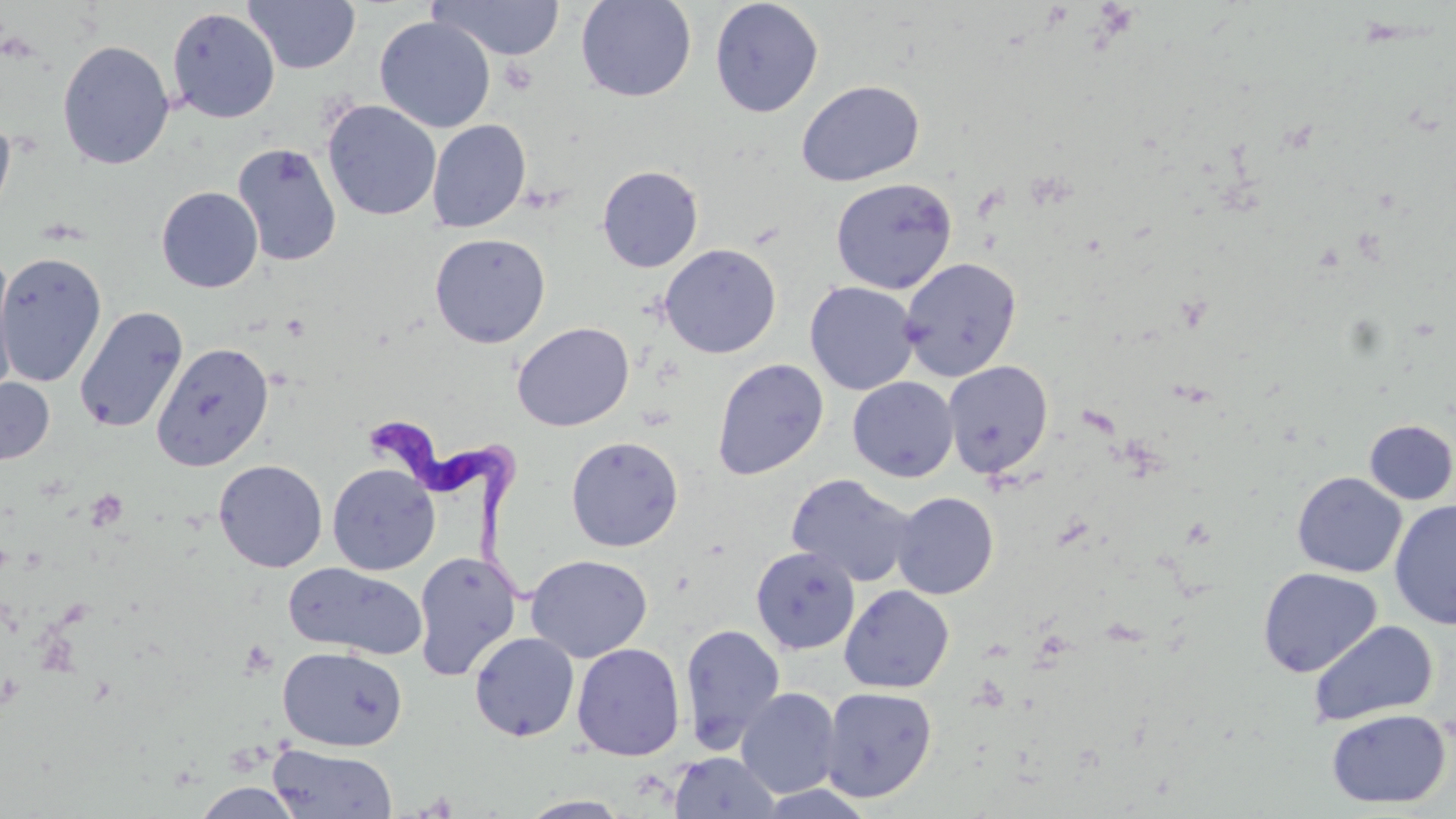

Summary:
  - Coordinate format: approximate bounding boxes as [x1, y1, x2, y2] in pixels
  - Uninfected red blood cell locations: [243, 0, 360, 74], [576, 0, 696, 102], [709, 0, 824, 117], [429, 1, 566, 61], [167, 7, 280, 124], [374, 16, 496, 133], [57, 39, 175, 170], [796, 80, 924, 186], [322, 101, 441, 221], [0, 110, 16, 228], [427, 119, 531, 233], [231, 143, 343, 266], [597, 165, 704, 272], [831, 177, 957, 294], [156, 186, 263, 293], [429, 232, 551, 348], [660, 244, 781, 359], [0, 250, 107, 387], [0, 251, 19, 401], [899, 257, 1022, 382], [805, 281, 919, 395], [74, 306, 188, 434], [512, 322, 634, 431], [151, 342, 274, 471], [711, 358, 829, 480], [942, 360, 1053, 479], [0, 377, 55, 465], [847, 377, 959, 482], [1364, 419, 1456, 505], [566, 435, 684, 552], [213, 459, 328, 572], [327, 463, 440, 576], [1292, 472, 1407, 578], [786, 473, 918, 588], [892, 491, 999, 599], [1389, 499, 1456, 630], [750, 546, 860, 654], [413, 551, 522, 681], [525, 554, 652, 662], [283, 563, 429, 658], [1258, 567, 1381, 678], [839, 585, 955, 693], [1308, 619, 1438, 726], [679, 623, 786, 752], [469, 632, 580, 742], [571, 642, 685, 761], [278, 647, 408, 752], [820, 686, 938, 803], [736, 687, 841, 797], [1326, 709, 1451, 808], [268, 744, 398, 818], [668, 751, 782, 818], [192, 782, 305, 818], [519, 795, 633, 818]
  - Trypanosoma brucei locations: [351, 415, 539, 601]
  - Platelet locations: [500, 59, 537, 95], [281, 314, 311, 342], [85, 490, 129, 532], [240, 639, 279, 678]
  - Slide-level diagnosis: Trypanosoma brucei
  - Modality: light microscopy
  - Preparation: thin blood smear
  - Image size: 1456×819 pixels
  - Magnification: 1000x
  - Field of view: single
  - Stain: May-Grünwald-Giemsa